Locate every blood parasite and identify its species.
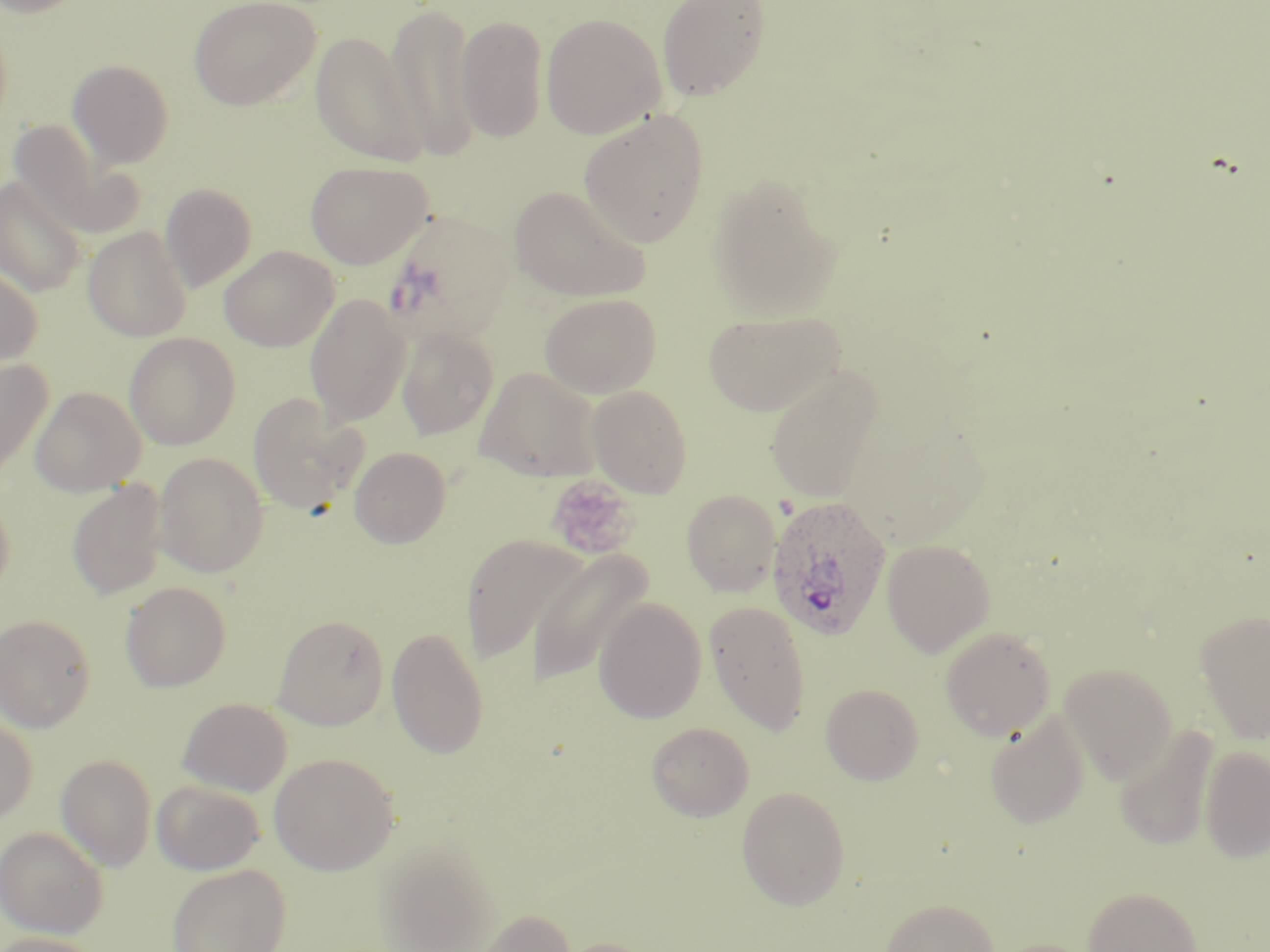
Approximate bounding boxes as [x1, y1, x2, y2] in pixels.
Plasmodium ovale-infected red blood cells: [766, 495, 892, 640].
No Plasmodium falciparum, Plasmodium malariae, Plasmodium vivax, Babesia divergens, or Trypanosoma brucei observed.

Summary:
  - Platelet locations: [545, 474, 639, 559]
  - Uninfected red blood cell locations: [0, 0, 90, 19], [188, 0, 321, 110], [656, 0, 771, 102], [384, 2, 479, 162], [540, 13, 666, 139], [456, 14, 548, 142], [309, 31, 429, 166], [67, 60, 174, 168], [578, 108, 709, 248], [8, 119, 142, 239], [305, 160, 433, 269], [708, 173, 844, 320], [0, 175, 87, 297], [160, 182, 257, 292], [509, 185, 650, 302], [381, 209, 514, 345], [82, 226, 192, 342], [219, 245, 338, 351], [0, 263, 43, 372], [540, 292, 661, 398], [304, 293, 411, 425], [703, 308, 845, 417], [396, 326, 498, 439], [123, 332, 241, 450], [0, 357, 53, 476], [764, 365, 885, 504], [473, 366, 602, 482], [586, 384, 692, 498], [30, 385, 146, 496], [247, 392, 367, 515], [349, 446, 451, 549], [153, 451, 269, 577], [66, 479, 169, 601], [0, 486, 15, 600], [683, 490, 780, 596], [459, 533, 590, 663], [881, 539, 996, 657], [525, 548, 652, 688], [120, 581, 231, 692], [593, 598, 708, 724], [703, 601, 811, 736], [1195, 609, 1270, 745], [0, 614, 95, 732], [272, 614, 389, 730], [940, 625, 1056, 741], [386, 627, 489, 759], [1059, 663, 1177, 785], [820, 683, 923, 784], [177, 697, 292, 796], [985, 711, 1090, 829], [0, 714, 37, 825], [646, 722, 754, 821], [1114, 726, 1219, 850], [1199, 746, 1270, 863], [268, 752, 399, 875], [56, 754, 157, 871], [151, 779, 265, 875], [736, 785, 851, 910], [0, 826, 109, 938], [372, 839, 502, 952], [167, 863, 292, 952], [1082, 885, 1202, 952], [880, 898, 999, 952], [472, 909, 576, 952], [0, 932, 106, 952], [551, 937, 662, 952]
  - Slide-level diagnosis: Plasmodium ovale
  - Field of view: one of a larger specimen
  - Image size: 1270×952 pixels
  - Modality: light microscopy
  - Preparation: thin blood smear
  - Magnification: 1000x
  - Stain: May-Grünwald-Giemsa